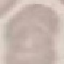
result: negative for malaria parasites
capture: smartphone camera at the microscope eyepiece
stain: Giemsa
preparation: thin blood film
image_type: automatically extracted cell patch, resized to 64 × 64 pixels